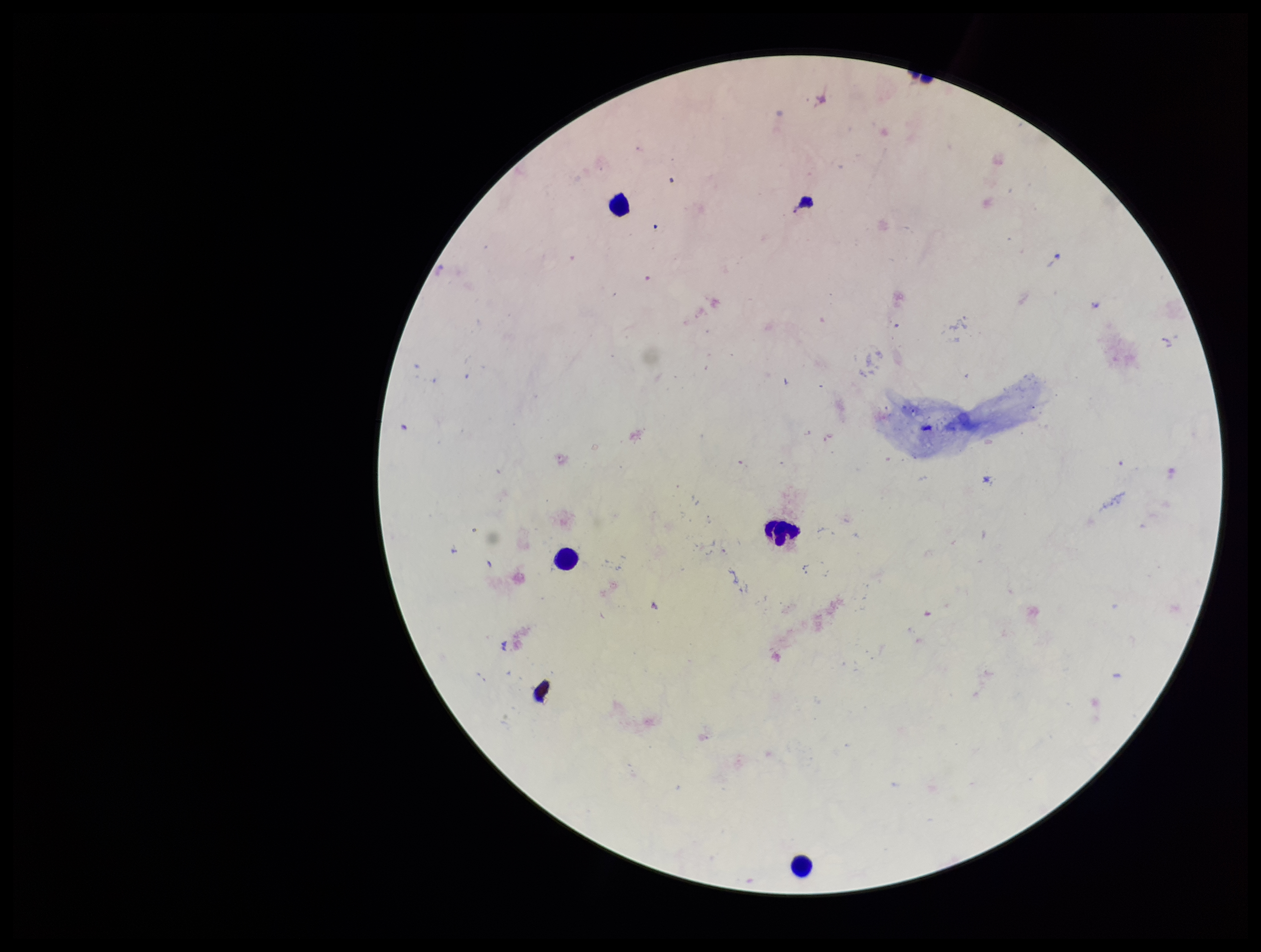

Summary:
  - Plasmodium parasites: none seen
  - Patient malaria status: negative
  - Capture: smartphone photograph through the microscope eyepiece
  - Field of view: one from this slide
  - Image size: 1261×952 pixels
  - Parasite count: 0
  - Stain: Giemsa
  - Preparation: thick blood smear
  - Leukocyte count: 4